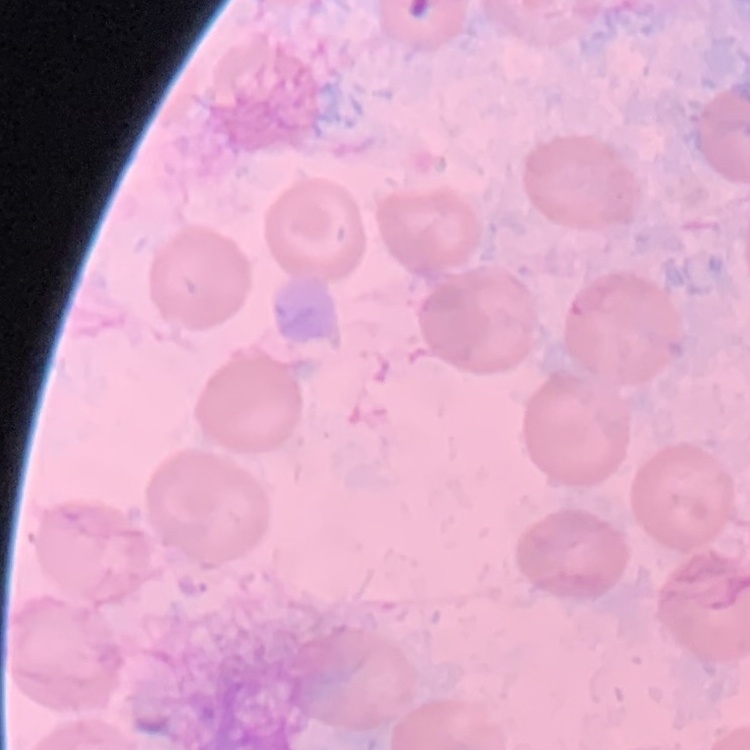 The erythrocytes show no rouleaux formation. Thin blood film. Field's or Giemsa stain. Square crop of a larger photomicrograph.